State which parasite is depicted.
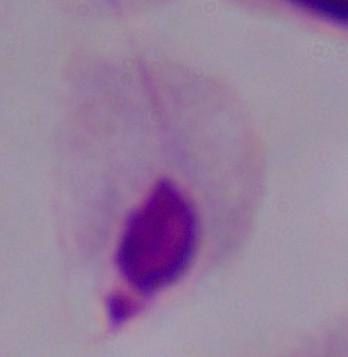

This is a trichomonad.

Micrograph. 1000x magnification.